Locate every leukocyte (white blood cell).
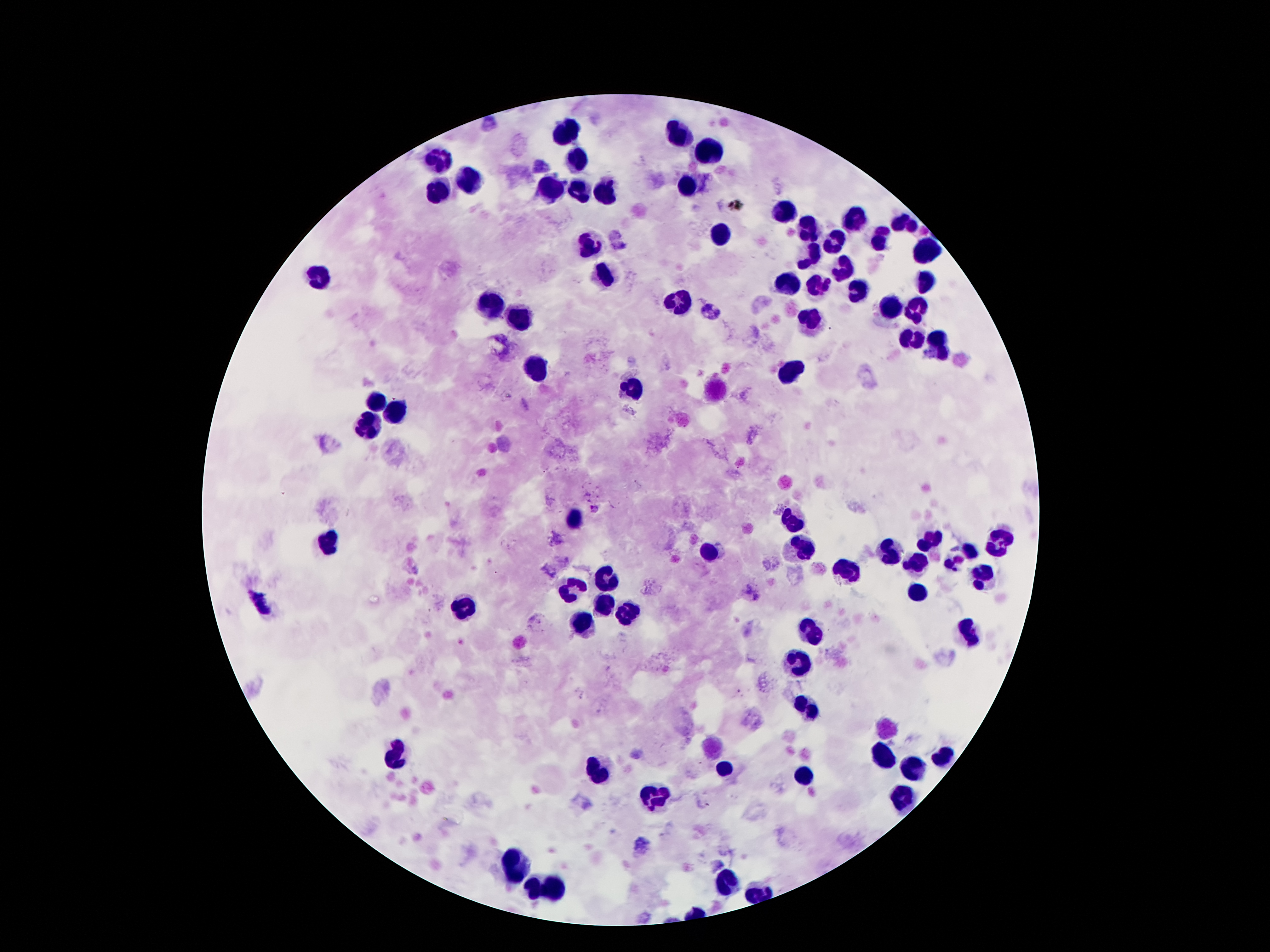
Approximate centers as (x, y) in pixels.
Leukocytes: (568, 131), (678, 134), (708, 154), (578, 161), (439, 162), (473, 179), (687, 186), (551, 188), (441, 191), (580, 193), (604, 195), (786, 212), (855, 220), (904, 224), (809, 227), (724, 234), (835, 240), (881, 240), (589, 243), (928, 252), (812, 256), (840, 267), (320, 273), (606, 273), (788, 278), (927, 283), (817, 290), (855, 293), (679, 303), (888, 306), (490, 307), (916, 310), (519, 321), (809, 322), (911, 337), (940, 348), (534, 366), (792, 373), (635, 391), (378, 398), (392, 410), (371, 427), (571, 520), (791, 522), (930, 539), (328, 546), (998, 548), (803, 551), (710, 552), (888, 553), (960, 555), (914, 565), (846, 570), (982, 577), (606, 580), (571, 588), (919, 590), (603, 606), (462, 611), (629, 614), (581, 620), (815, 634), (966, 634), (798, 663), (807, 708), (398, 754), (885, 757), (943, 758), (727, 767), (913, 767), (597, 770), (803, 776), (656, 797), (901, 800), (516, 867), (725, 884), (542, 889).

Plasmodium parasite locations = (595, 509)
stain = Giemsa
magnification = 100x
image size = 1270×952 pixels
preparation = thick blood film
field of view = one from this slide
capture = smartphone camera through the microscope eyepiece
patient malaria status = infected with Plasmodium falciparum